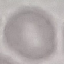

result = negative for malaria parasites
stain = Giemsa
preparation = thin blood smear
image type = cell patch, automatically extracted from a larger field of view and resized to 64 × 64 pixels
capture = smartphone camera at the microscope eyepiece